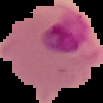 Segmented cell region on a black background. From a thin blood film. Image is 103×103 pixels. Malaria status: parasitized.